Identify the blood parasite species.
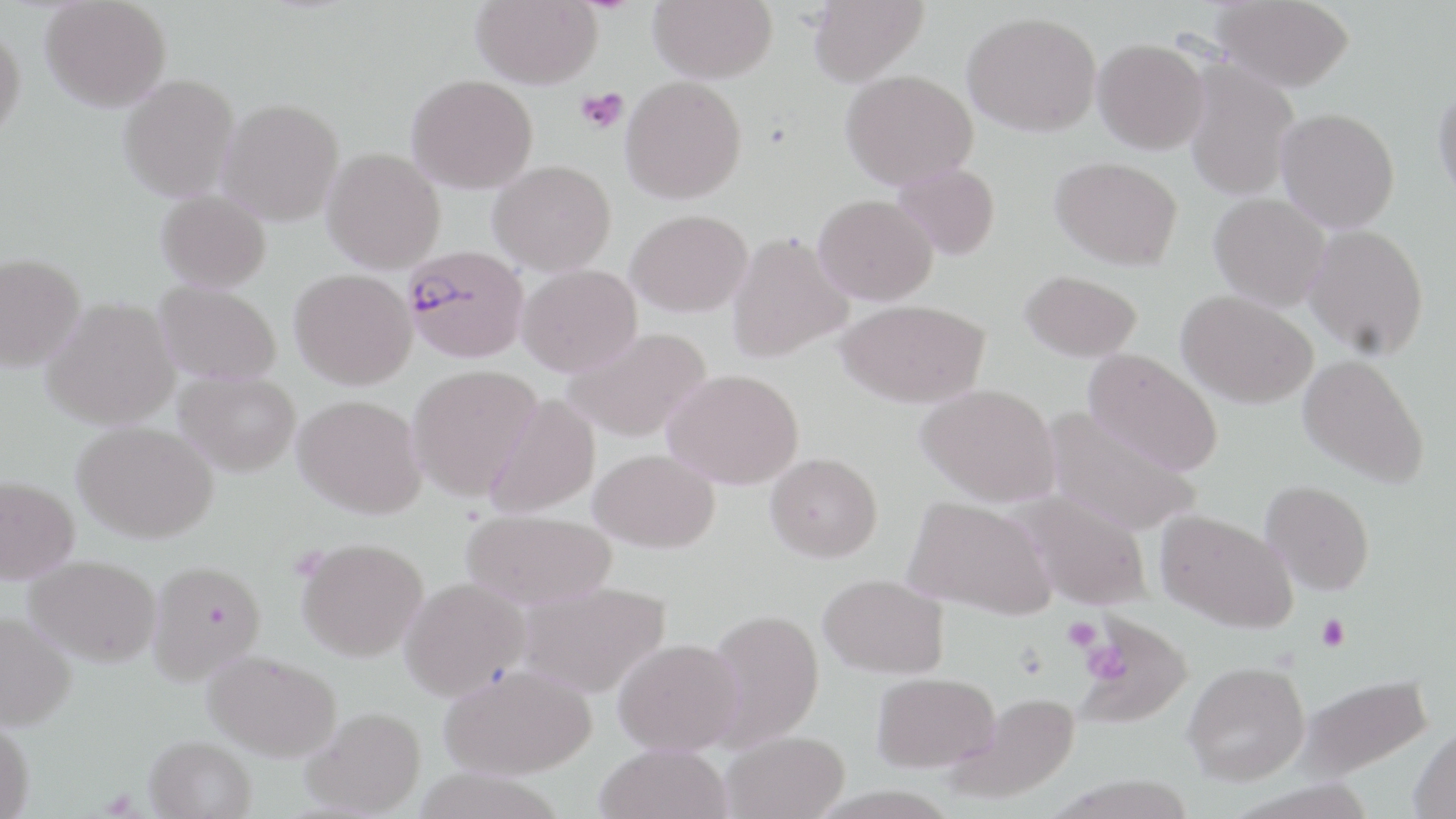
Plasmodium falciparum.

modality = light microscopy
magnification = 1000x
Plasmodium falciparum-infected red blood cell locations = approximate bounding boxes as (x1,y1)-(x2,y2) corner pairs in pixels: (402,245)-(530,363)
preparation = thin blood smear
field of view = single
image size = 1456×819 pixels
platelet locations = approximate bounding boxes as (x1,y1)-(x2,y2) corner pairs in pixels: (576,88)-(628,133), (1316,613)-(1351,652), (1063,615)-(1101,652), (1080,640)-(1132,687)
uninfected red blood cell locations = approximate bounding boxes as (x1,y1)-(x2,y2) corner pairs in pixels: (41,0)-(171,112), (472,0)-(603,88), (648,0)-(777,83), (807,0)-(929,87), (1213,0)-(1355,91), (963,11)-(1101,136), (0,21)-(26,144), (1093,38)-(1209,154), (1183,60)-(1300,202), (841,69)-(978,189), (118,74)-(240,202), (406,74)-(538,193), (620,75)-(747,204), (1432,80)-(1456,209), (217,98)-(345,226), (1276,108)-(1400,232), (322,147)-(445,274), (1050,156)-(1183,270), (488,159)-(616,275), (892,162)-(1001,260), (156,189)-(271,292), (1209,193)-(1331,311), (814,194)-(938,305), (625,209)-(752,317), (1304,224)-(1430,360), (726,232)-(853,362), (0,253)-(85,372), (517,263)-(642,377), (289,268)-(417,389), (1019,269)-(1143,361), (153,281)-(282,385), (1176,290)-(1318,408), (42,297)-(179,429), (837,299)-(989,408), (562,327)-(712,443), (1082,348)-(1224,475), (1298,353)-(1431,489), (407,364)-(542,500), (663,368)-(804,489), (175,370)-(301,476), (917,383)-(1060,506), (483,393)-(600,519), (293,394)-(427,519), (1043,407)-(1202,537), (73,420)-(218,542), (589,448)-(719,553), (765,452)-(882,562), (0,476)-(80,583), (1260,480)-(1375,595), (1012,490)-(1153,610), (903,496)-(1056,618), (462,509)-(616,609), (1155,509)-(1298,633), (297,537)-(428,661), (25,554)-(161,666), (147,559)-(266,683), (819,573)-(949,678), (400,577)-(531,699), (515,580)-(672,698), (704,608)-(825,749), (0,611)-(76,730), (1075,615)-(1190,728), (613,637)-(744,755), (204,650)-(342,761), (1182,660)-(1310,785), (439,663)-(597,779), (871,671)-(1000,773), (1294,672)-(1435,782), (949,692)-(1083,803), (303,706)-(426,817), (0,718)-(34,818), (1411,721)-(1456,819), (721,730)-(849,819), (145,735)-(257,819), (594,743)-(733,819)
stain = May-Grünwald-Giemsa